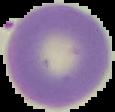
{
  "result": "no Plasmodium parasites detected",
  "image_size": "115×112 pixels",
  "preparation": "thin blood film",
  "image_type": "segmented cell region on a black background"
}